Locate and identify every blood parasite.
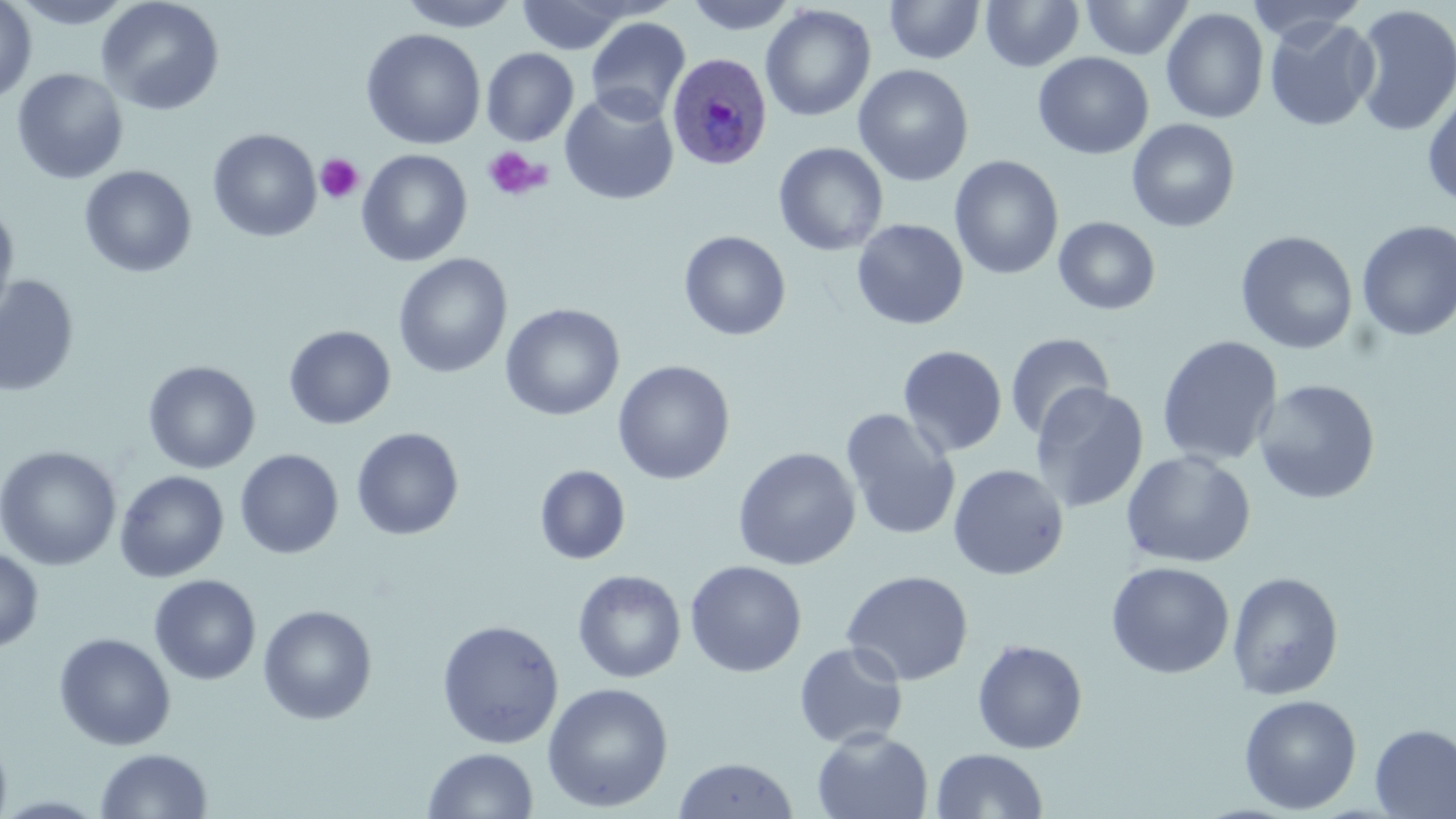

Approximate bounding boxes as named x1/y1/x2/y2 corners in pixels.
Plasmodium ovale-infected red blood cells: (x1=666, y1=51, x2=773, y2=172).
No Plasmodium falciparum, Plasmodium malariae, Plasmodium vivax, Babesia divergens, or Trypanosoma brucei observed.

Summary:
  - Platelet locations: (x1=481, y1=146, x2=551, y2=202), (x1=315, y1=154, x2=363, y2=204)
  - Uninfected red blood cell locations: (x1=0, y1=0, x2=37, y2=105), (x1=8, y1=0, x2=137, y2=29), (x1=96, y1=0, x2=225, y2=116), (x1=399, y1=0, x2=520, y2=31), (x1=517, y1=0, x2=631, y2=54), (x1=683, y1=0, x2=798, y2=35), (x1=981, y1=0, x2=1084, y2=72), (x1=1081, y1=0, x2=1193, y2=60), (x1=1246, y1=0, x2=1367, y2=46), (x1=884, y1=1, x2=985, y2=64), (x1=760, y1=4, x2=876, y2=122), (x1=1352, y1=4, x2=1456, y2=137), (x1=1161, y1=7, x2=1269, y2=124), (x1=585, y1=16, x2=691, y2=124), (x1=1264, y1=17, x2=1380, y2=132), (x1=360, y1=28, x2=486, y2=150), (x1=481, y1=48, x2=579, y2=147), (x1=1033, y1=52, x2=1154, y2=159), (x1=853, y1=64, x2=974, y2=187), (x1=11, y1=68, x2=128, y2=185), (x1=1422, y1=86, x2=1456, y2=210), (x1=559, y1=91, x2=679, y2=206), (x1=1127, y1=118, x2=1241, y2=232), (x1=207, y1=128, x2=322, y2=243), (x1=773, y1=142, x2=888, y2=256), (x1=356, y1=149, x2=473, y2=266), (x1=949, y1=156, x2=1064, y2=280), (x1=79, y1=165, x2=197, y2=278), (x1=0, y1=201, x2=19, y2=332), (x1=1053, y1=216, x2=1161, y2=316), (x1=851, y1=218, x2=969, y2=330), (x1=1356, y1=220, x2=1456, y2=342), (x1=679, y1=230, x2=791, y2=341), (x1=1235, y1=230, x2=1359, y2=355), (x1=393, y1=253, x2=512, y2=378), (x1=0, y1=275, x2=80, y2=398), (x1=500, y1=303, x2=625, y2=421), (x1=283, y1=324, x2=396, y2=430), (x1=1004, y1=333, x2=1114, y2=441), (x1=1156, y1=335, x2=1283, y2=468), (x1=897, y1=345, x2=1007, y2=457), (x1=142, y1=360, x2=261, y2=474), (x1=612, y1=360, x2=735, y2=485), (x1=1253, y1=379, x2=1381, y2=505), (x1=1029, y1=382, x2=1149, y2=514), (x1=840, y1=408, x2=961, y2=542), (x1=350, y1=427, x2=465, y2=541), (x1=0, y1=445, x2=122, y2=571), (x1=732, y1=447, x2=861, y2=571), (x1=234, y1=449, x2=344, y2=559), (x1=1120, y1=450, x2=1256, y2=569), (x1=948, y1=463, x2=1069, y2=580), (x1=535, y1=464, x2=631, y2=565), (x1=114, y1=470, x2=229, y2=582), (x1=0, y1=548, x2=44, y2=653), (x1=685, y1=560, x2=807, y2=678), (x1=1105, y1=561, x2=1235, y2=679), (x1=573, y1=569, x2=686, y2=683), (x1=841, y1=569, x2=974, y2=686), (x1=1227, y1=571, x2=1344, y2=700), (x1=149, y1=574, x2=261, y2=685), (x1=258, y1=605, x2=377, y2=725), (x1=436, y1=619, x2=564, y2=749), (x1=53, y1=632, x2=176, y2=751), (x1=972, y1=639, x2=1088, y2=754), (x1=794, y1=642, x2=908, y2=749), (x1=542, y1=682, x2=674, y2=813), (x1=1239, y1=694, x2=1361, y2=814), (x1=1370, y1=724, x2=1456, y2=818), (x1=812, y1=729, x2=934, y2=819), (x1=0, y1=733, x2=12, y2=819), (x1=423, y1=747, x2=538, y2=819), (x1=94, y1=748, x2=213, y2=819), (x1=931, y1=748, x2=1048, y2=818), (x1=672, y1=757, x2=798, y2=818)
  - Slide-level diagnosis: Plasmodium ovale
  - Preparation: thin blood film
  - Magnification: 1000x
  - Field of view: one of a larger specimen
  - Modality: light microscopy
  - Stain: May-Grünwald-Giemsa
  - Image size: 1456×819 pixels